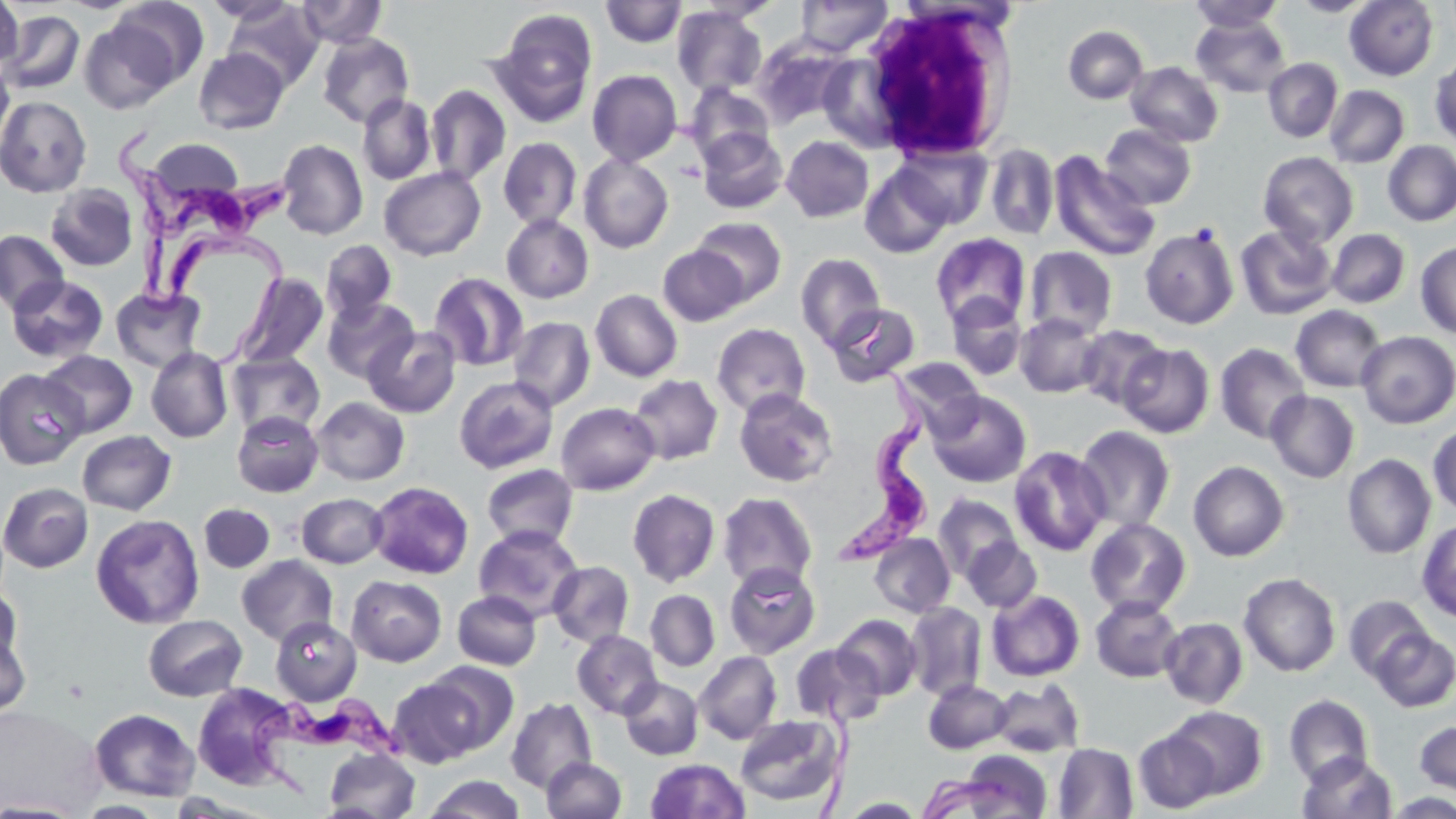

Summary:
  - Coordinate format: approximate bounding boxes as named x1/y1/x2/y2 corners in pixels
  - Trypanosoma brucei locations: (x1=117, y1=122, x2=300, y2=242), (x1=135, y1=223, x2=291, y2=363), (x1=838, y1=354, x2=930, y2=569), (x1=245, y1=694, x2=412, y2=806)
  - Uninfected red blood cell locations: (x1=0, y1=0, x2=23, y2=73), (x1=113, y1=0, x2=209, y2=88), (x1=202, y1=0, x2=302, y2=26), (x1=297, y1=0, x2=387, y2=48), (x1=694, y1=0, x2=783, y2=23), (x1=796, y1=0, x2=892, y2=56), (x1=601, y1=1, x2=686, y2=47), (x1=1188, y1=1, x2=1285, y2=32), (x1=1290, y1=1, x2=1376, y2=17), (x1=1345, y1=1, x2=1438, y2=81), (x1=224, y1=3, x2=323, y2=91), (x1=671, y1=6, x2=767, y2=97), (x1=1, y1=10, x2=85, y2=95), (x1=492, y1=14, x2=597, y2=126), (x1=1191, y1=15, x2=1291, y2=98), (x1=80, y1=19, x2=180, y2=114), (x1=1063, y1=25, x2=1148, y2=104), (x1=317, y1=33, x2=414, y2=128), (x1=752, y1=38, x2=849, y2=129), (x1=194, y1=48, x2=289, y2=134), (x1=1430, y1=57, x2=1456, y2=146), (x1=1263, y1=58, x2=1342, y2=143), (x1=0, y1=60, x2=14, y2=155), (x1=1126, y1=62, x2=1224, y2=147), (x1=587, y1=69, x2=683, y2=166), (x1=684, y1=83, x2=775, y2=166), (x1=426, y1=85, x2=511, y2=185), (x1=1324, y1=85, x2=1409, y2=168), (x1=357, y1=94, x2=435, y2=185), (x1=0, y1=96, x2=92, y2=197), (x1=1100, y1=124, x2=1196, y2=209), (x1=698, y1=128, x2=788, y2=214), (x1=781, y1=135, x2=874, y2=223), (x1=498, y1=137, x2=582, y2=230), (x1=148, y1=139, x2=243, y2=201), (x1=277, y1=139, x2=368, y2=240), (x1=1383, y1=141, x2=1456, y2=225), (x1=984, y1=143, x2=1059, y2=240), (x1=896, y1=144, x2=991, y2=228), (x1=1258, y1=151, x2=1359, y2=248), (x1=1049, y1=152, x2=1160, y2=261), (x1=579, y1=153, x2=673, y2=253), (x1=860, y1=165, x2=954, y2=258), (x1=379, y1=167, x2=485, y2=261), (x1=46, y1=184, x2=138, y2=271), (x1=501, y1=214, x2=594, y2=303), (x1=690, y1=217, x2=787, y2=305), (x1=1235, y1=224, x2=1337, y2=320), (x1=1140, y1=225, x2=1239, y2=330), (x1=1327, y1=229, x2=1410, y2=308), (x1=0, y1=231, x2=69, y2=316), (x1=931, y1=233, x2=1030, y2=328), (x1=321, y1=240, x2=397, y2=324), (x1=1415, y1=242, x2=1456, y2=339), (x1=658, y1=245, x2=748, y2=325), (x1=1024, y1=246, x2=1119, y2=339), (x1=796, y1=253, x2=886, y2=350), (x1=233, y1=272, x2=329, y2=370), (x1=428, y1=272, x2=529, y2=372), (x1=6, y1=275, x2=108, y2=363), (x1=110, y1=286, x2=207, y2=373), (x1=591, y1=289, x2=683, y2=382), (x1=946, y1=294, x2=1027, y2=381), (x1=322, y1=297, x2=419, y2=384), (x1=826, y1=303, x2=921, y2=386), (x1=1291, y1=305, x2=1387, y2=393), (x1=1015, y1=313, x2=1105, y2=398), (x1=508, y1=316, x2=595, y2=412), (x1=712, y1=323, x2=811, y2=417), (x1=1075, y1=324, x2=1168, y2=411), (x1=362, y1=326, x2=461, y2=418), (x1=1356, y1=331, x2=1456, y2=428), (x1=1118, y1=343, x2=1214, y2=438), (x1=1215, y1=343, x2=1311, y2=443), (x1=146, y1=347, x2=233, y2=443), (x1=40, y1=350, x2=137, y2=438), (x1=227, y1=352, x2=325, y2=437), (x1=893, y1=357, x2=984, y2=433), (x1=0, y1=369, x2=87, y2=469), (x1=628, y1=374, x2=722, y2=465), (x1=454, y1=376, x2=558, y2=474), (x1=734, y1=388, x2=838, y2=487), (x1=927, y1=390, x2=1031, y2=488), (x1=1266, y1=390, x2=1359, y2=483), (x1=312, y1=397, x2=409, y2=485), (x1=556, y1=402, x2=659, y2=495), (x1=232, y1=410, x2=323, y2=497), (x1=1428, y1=423, x2=1456, y2=516), (x1=1074, y1=425, x2=1175, y2=532), (x1=77, y1=430, x2=177, y2=515), (x1=1009, y1=445, x2=1111, y2=556), (x1=1342, y1=454, x2=1436, y2=559), (x1=1188, y1=461, x2=1289, y2=561), (x1=481, y1=464, x2=579, y2=550), (x1=368, y1=481, x2=474, y2=579), (x1=0, y1=482, x2=92, y2=572), (x1=627, y1=489, x2=721, y2=587), (x1=717, y1=492, x2=818, y2=591), (x1=297, y1=493, x2=388, y2=568), (x1=933, y1=494, x2=1022, y2=582), (x1=199, y1=503, x2=275, y2=573), (x1=91, y1=513, x2=205, y2=629), (x1=1085, y1=518, x2=1191, y2=618), (x1=1417, y1=520, x2=1456, y2=621), (x1=473, y1=525, x2=584, y2=622), (x1=869, y1=533, x2=955, y2=618), (x1=962, y1=538, x2=1041, y2=612), (x1=237, y1=555, x2=338, y2=646), (x1=547, y1=560, x2=635, y2=648), (x1=724, y1=562, x2=821, y2=658), (x1=1239, y1=572, x2=1341, y2=677), (x1=346, y1=575, x2=447, y2=666), (x1=0, y1=585, x2=24, y2=674), (x1=645, y1=589, x2=720, y2=672), (x1=987, y1=590, x2=1085, y2=681), (x1=453, y1=591, x2=541, y2=670), (x1=1091, y1=596, x2=1184, y2=682), (x1=1344, y1=596, x2=1431, y2=682), (x1=904, y1=603, x2=987, y2=700), (x1=143, y1=614, x2=247, y2=701), (x1=833, y1=614, x2=922, y2=700), (x1=270, y1=616, x2=362, y2=705), (x1=1159, y1=617, x2=1248, y2=709), (x1=0, y1=624, x2=31, y2=721), (x1=1370, y1=629, x2=1456, y2=713), (x1=572, y1=630, x2=662, y2=719), (x1=791, y1=644, x2=885, y2=727), (x1=694, y1=651, x2=782, y2=744), (x1=421, y1=661, x2=517, y2=755), (x1=388, y1=676, x2=488, y2=767), (x1=619, y1=677, x2=703, y2=760), (x1=923, y1=679, x2=1012, y2=754), (x1=990, y1=679, x2=1085, y2=757), (x1=192, y1=683, x2=298, y2=789), (x1=1283, y1=695, x2=1373, y2=787), (x1=506, y1=696, x2=597, y2=794), (x1=1165, y1=705, x2=1268, y2=799), (x1=89, y1=708, x2=200, y2=802), (x1=734, y1=714, x2=845, y2=808), (x1=1415, y1=720, x2=1456, y2=796), (x1=1133, y1=729, x2=1221, y2=813), (x1=1053, y1=743, x2=1139, y2=818), (x1=324, y1=747, x2=420, y2=817), (x1=960, y1=751, x2=1053, y2=818), (x1=1298, y1=752, x2=1396, y2=818), (x1=542, y1=757, x2=626, y2=818), (x1=645, y1=758, x2=750, y2=818), (x1=917, y1=773, x2=1007, y2=819), (x1=423, y1=774, x2=526, y2=819), (x1=1384, y1=792, x2=1456, y2=818), (x1=841, y1=797, x2=926, y2=817), (x1=0, y1=800, x2=87, y2=818), (x1=74, y1=801, x2=170, y2=818)
  - White blood cell locations: (x1=857, y1=2, x2=1021, y2=160)
  - Slide-level diagnosis: Trypanosoma brucei
  - Field of view: one of a larger specimen
  - Modality: light microscopy
  - Magnification: 1000x
  - Image size: 1456×819 pixels
  - Stain: May-Grünwald-Giemsa
  - Preparation: thin blood smear